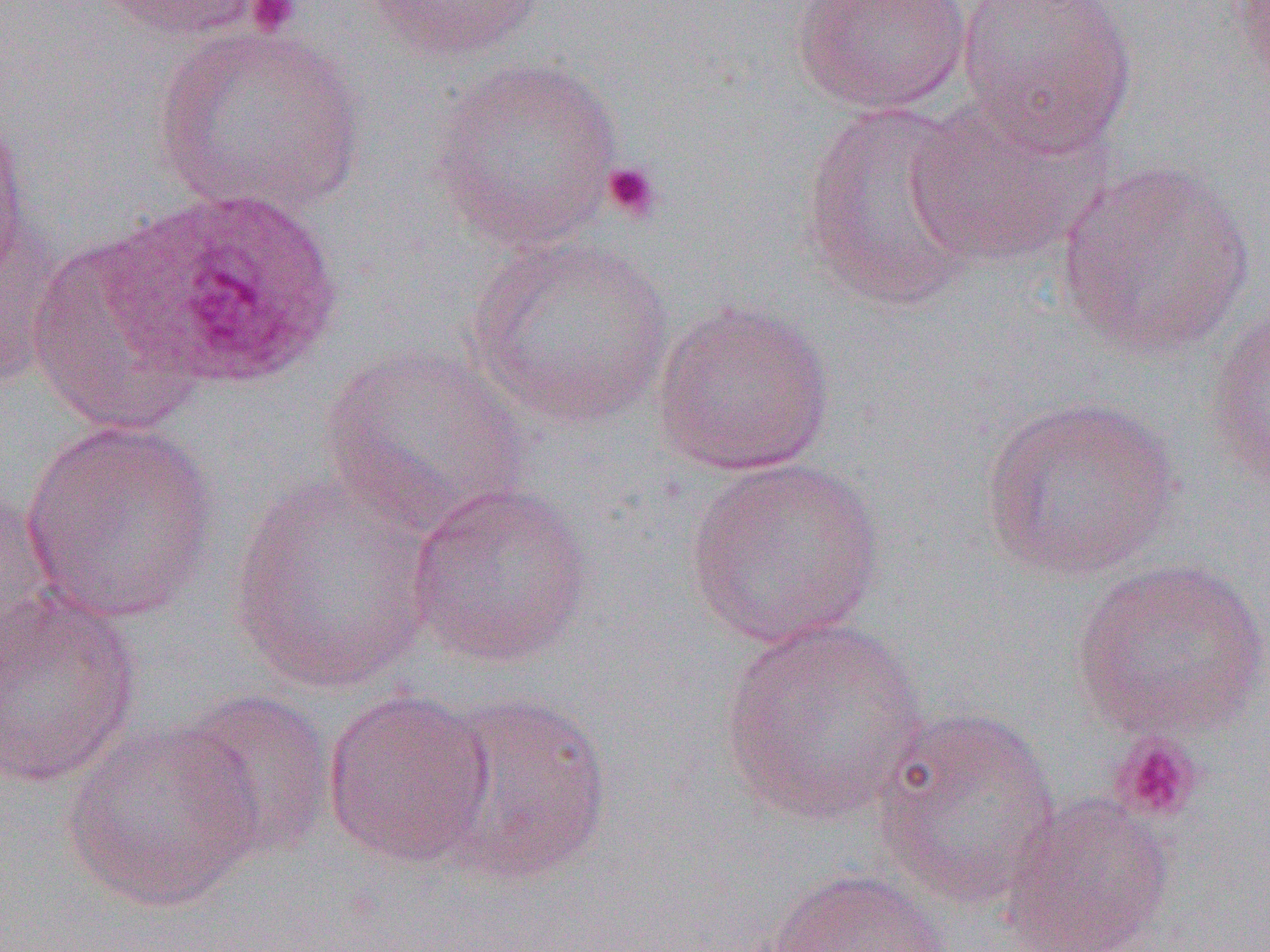
{
  "slide_level_diagnosis": "Plasmodium ovale",
  "uninfected_red_blood_cell_locations": "approximate bounding boxes as [x1, y1, x2, y2] in pixels: [94, 0, 274, 42], [359, 0, 550, 66], [790, 0, 974, 115], [955, 0, 1138, 158], [1228, 0, 1270, 97], [153, 22, 367, 219], [430, 55, 625, 253], [906, 95, 1109, 270], [799, 100, 986, 314], [0, 108, 34, 299], [1054, 159, 1257, 362], [0, 193, 68, 392], [464, 232, 676, 428], [27, 233, 210, 437], [649, 299, 836, 477], [1203, 301, 1270, 493], [320, 341, 531, 537], [978, 394, 1185, 582], [18, 419, 222, 624], [682, 455, 887, 648], [228, 473, 439, 696], [0, 480, 55, 668], [407, 482, 594, 669], [1070, 557, 1269, 741], [0, 587, 143, 789], [717, 618, 931, 826], [323, 688, 495, 869], [172, 689, 337, 861], [426, 689, 615, 887], [871, 706, 1062, 912], [63, 720, 268, 914], [999, 793, 1175, 952], [763, 868, 953, 952]",
  "image_size": "1270×952 pixels",
  "platelet_locations": "approximate bounding boxes as [x1, y1, x2, y2] in pixels: [245, 0, 302, 36], [601, 160, 663, 224], [1108, 732, 1205, 824]",
  "plasmodium_ovale_infected_red_blood_cell_locations": "approximate bounding boxes as [x1, y1, x2, y2] in pixels: [104, 186, 347, 392]",
  "field_of_view": "single",
  "preparation": "thin blood smear",
  "modality": "optical microscopy",
  "magnification": "1000x"
}